Report the malaria status of this cell.
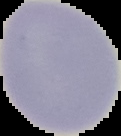
It is uninfected.

Summary:
  - Image size: 121×136 pixels
  - Image type: cell region segmented out of the field of view; surrounding area masked to black
  - Preparation: thin blood film